Name the parasite shown.
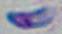

Toxoplasma gondii.

{
  "modality": "micrograph",
  "magnification": "1000x"
}